Locate every Plasmodium falciparum-infected red blood cell.
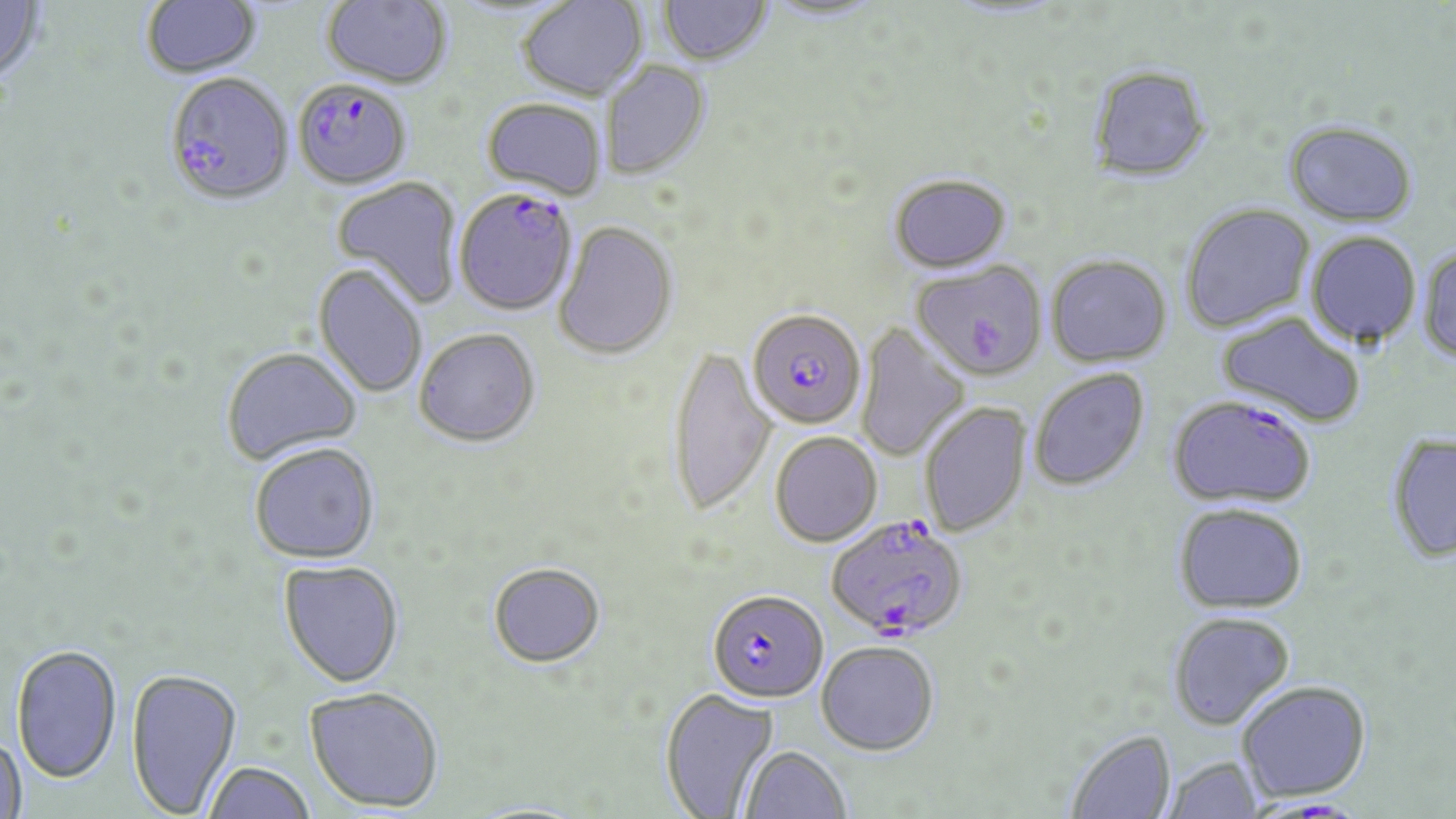
Approximate bounding boxes as named x1/y1/x2/y2 corners in pixels.
Plasmodium falciparum-infected red blood cells: (x1=165, y1=69, x2=295, y2=206), (x1=302, y1=81, x2=408, y2=192), (x1=454, y1=186, x2=579, y2=316), (x1=747, y1=308, x2=866, y2=429), (x1=1167, y1=394, x2=1317, y2=508), (x1=826, y1=513, x2=969, y2=641), (x1=707, y1=589, x2=829, y2=703).

Uninfected red blood cell locations: (x1=0, y1=0, x2=47, y2=87), (x1=141, y1=0, x2=261, y2=78), (x1=322, y1=0, x2=453, y2=88), (x1=517, y1=0, x2=648, y2=101), (x1=658, y1=1, x2=773, y2=66), (x1=763, y1=1, x2=887, y2=24), (x1=600, y1=61, x2=712, y2=180), (x1=1086, y1=64, x2=1212, y2=183), (x1=481, y1=97, x2=607, y2=200), (x1=1284, y1=120, x2=1419, y2=226), (x1=888, y1=173, x2=1012, y2=271), (x1=331, y1=176, x2=463, y2=308), (x1=1179, y1=202, x2=1316, y2=333), (x1=553, y1=220, x2=678, y2=360), (x1=1306, y1=231, x2=1422, y2=348), (x1=1418, y1=246, x2=1456, y2=365), (x1=1046, y1=254, x2=1172, y2=366), (x1=912, y1=260, x2=1046, y2=380), (x1=313, y1=263, x2=428, y2=399), (x1=1216, y1=311, x2=1367, y2=428), (x1=856, y1=322, x2=970, y2=462), (x1=415, y1=328, x2=541, y2=446), (x1=667, y1=344, x2=777, y2=517), (x1=221, y1=347, x2=363, y2=464), (x1=1029, y1=368, x2=1150, y2=491), (x1=919, y1=401, x2=1031, y2=537), (x1=770, y1=431, x2=882, y2=546), (x1=1387, y1=432, x2=1456, y2=563), (x1=249, y1=442, x2=381, y2=564), (x1=1172, y1=503, x2=1308, y2=613), (x1=278, y1=560, x2=405, y2=688), (x1=488, y1=561, x2=606, y2=667), (x1=1167, y1=611, x2=1295, y2=731), (x1=816, y1=640, x2=939, y2=755), (x1=11, y1=644, x2=123, y2=785), (x1=126, y1=668, x2=242, y2=817), (x1=1237, y1=680, x2=1371, y2=802), (x1=304, y1=686, x2=444, y2=812), (x1=660, y1=688, x2=779, y2=818), (x1=1064, y1=728, x2=1177, y2=818), (x1=0, y1=735, x2=26, y2=817), (x1=740, y1=745, x2=852, y2=818), (x1=1162, y1=755, x2=1265, y2=818), (x1=201, y1=761, x2=317, y2=819). Slide-level diagnosis: Plasmodium falciparum. Captured at 1000x magnification. Thin blood smear. Light microscopy. May-Grünwald-Giemsa stain. Image is 1456×819 pixels. One field of a larger specimen.